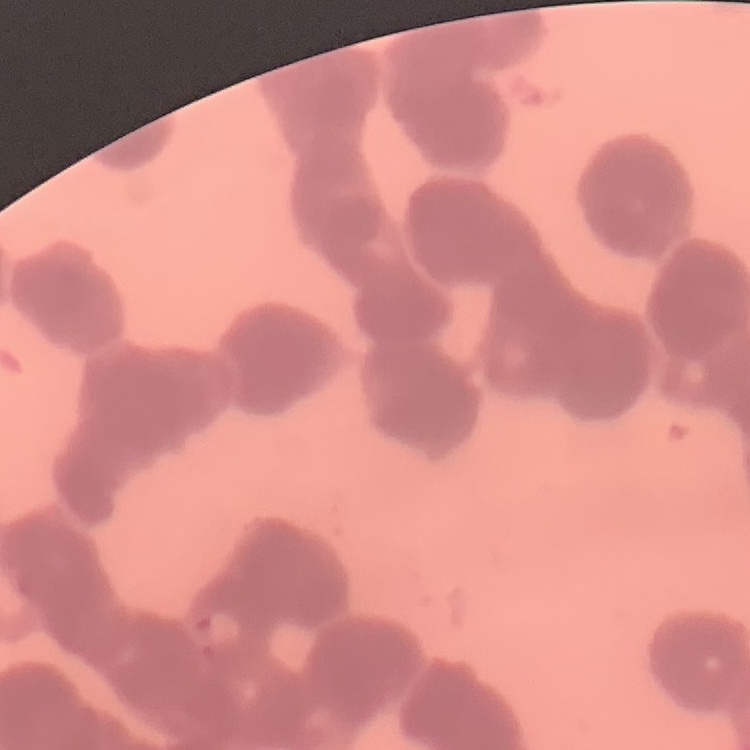
Summary:
  - Erythrocyte morphology: rouleaux formation
  - Preparation: thin peripheral smear
  - Image type: square crop of a larger photomicrograph
  - Stain: Field's or Giemsa